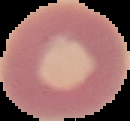

malaria status = uninfected
image size = 130×121 pixels
image type = segmented cell region with the area outside set to black
preparation = thin blood film